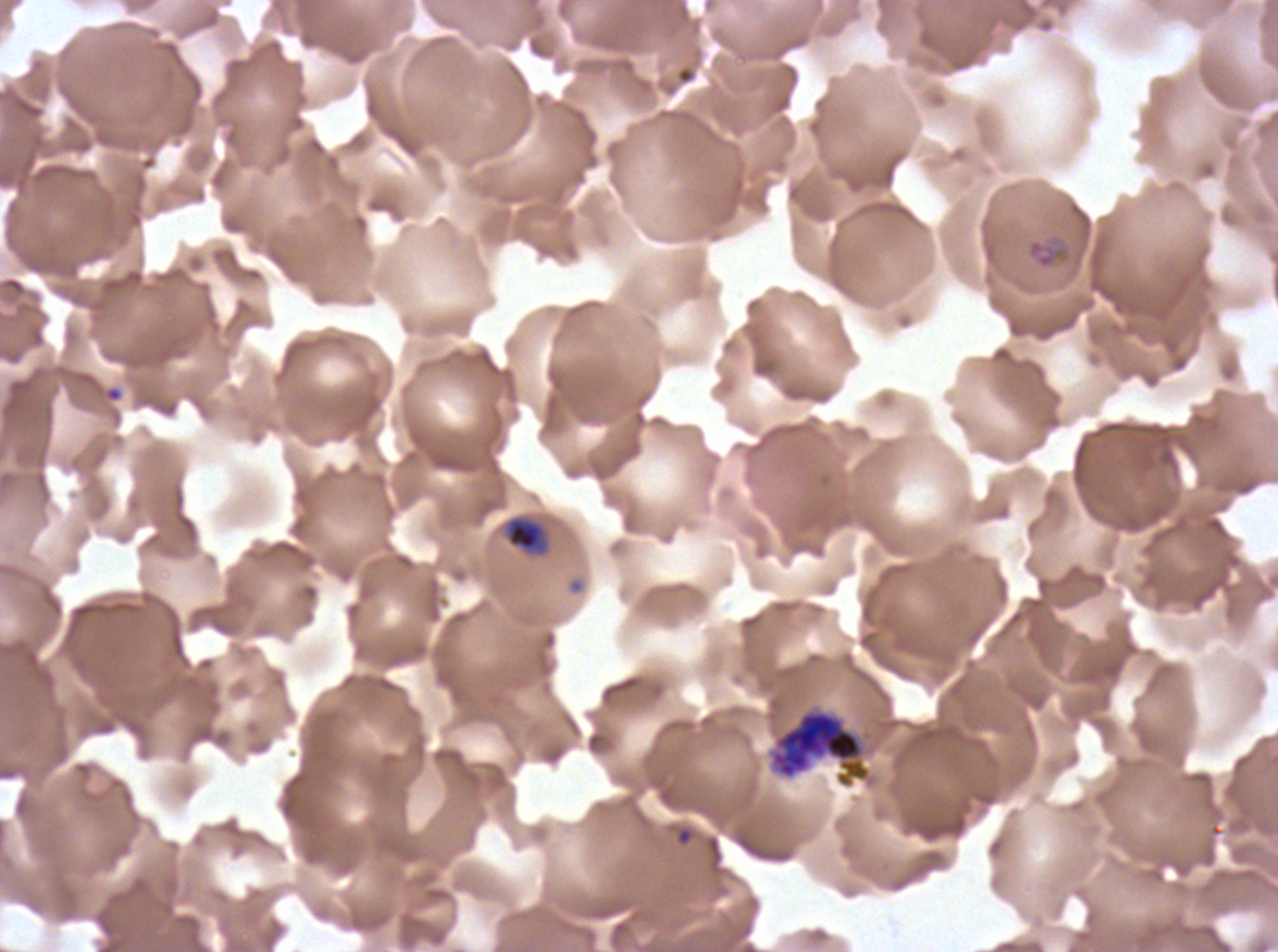

Approximate bounding rectangles given as corner coordinates in pixels from the top-left.
Summary:
  - Mid trophozoite locations: (x1=502, y1=515, x2=550, y2=557)
  - Ring locations: (x1=1026, y1=238, x2=1069, y2=269)
  - Early schizont locations: (x1=770, y1=710, x2=870, y2=787)
  - Field of view: sub-image separated from a larger composite
  - Preparation: thin blood film
  - Stain: Giemsa
  - Image size: 1278×952 pixels
  - Specimen: P. falciparum cultured ex vivo for 24 to 48 hours, from a patient in The Gambia
  - Life-cycle stages observed: ring, mid trophozoite, early schizont